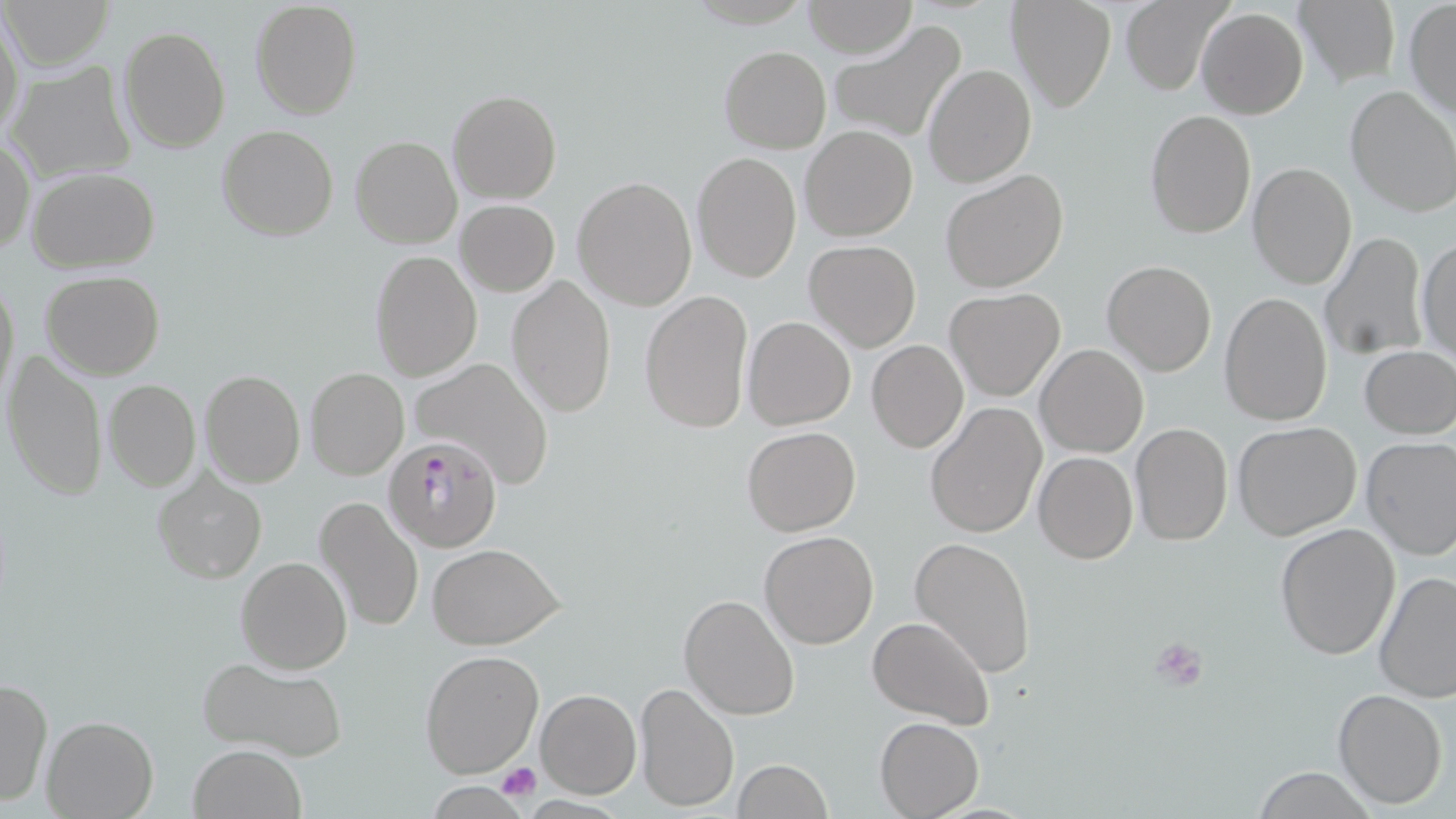 Approximate bounding boxes as (x1, y1, x2, y2) in pixels. Uninfected red blood cell locations: (3, 0, 115, 71), (1006, 0, 1117, 113), (1119, 0, 1229, 94), (1295, 0, 1399, 89), (250, 1, 362, 120), (802, 1, 917, 58), (1405, 2, 1455, 121), (1197, 7, 1308, 120), (0, 12, 24, 143), (826, 20, 968, 146), (118, 26, 231, 152), (718, 45, 831, 152), (5, 62, 137, 185), (923, 63, 1035, 187), (1344, 84, 1455, 218), (447, 89, 561, 204), (1143, 109, 1257, 239), (216, 125, 340, 241), (800, 126, 918, 242), (351, 136, 463, 250), (1, 139, 35, 256), (691, 151, 802, 284), (1247, 162, 1357, 289), (27, 167, 160, 273), (941, 170, 1069, 292), (573, 177, 697, 310), (456, 200, 559, 296), (1320, 232, 1428, 360), (1415, 237, 1455, 363), (804, 241, 921, 352), (370, 251, 483, 381), (1101, 260, 1217, 378), (40, 272, 164, 379), (506, 274, 616, 419), (1, 278, 19, 406), (944, 289, 1065, 401), (641, 290, 754, 437), (1219, 291, 1333, 427), (744, 317, 856, 430), (867, 340, 968, 452), (1035, 345, 1148, 459), (1360, 345, 1455, 440), (2, 348, 108, 502), (413, 358, 557, 483), (306, 367, 409, 479), (198, 369, 306, 488), (104, 380, 200, 491), (926, 403, 1046, 539), (1232, 421, 1362, 540), (1131, 423, 1233, 545), (742, 426, 861, 535), (1360, 436, 1456, 561), (1033, 451, 1138, 563), (151, 466, 266, 583), (315, 496, 424, 634), (1274, 521, 1402, 661), (758, 531, 879, 649), (909, 536, 1037, 676), (428, 543, 565, 648), (237, 554, 351, 674), (1373, 570, 1456, 706), (678, 593, 799, 720), (868, 617, 994, 729), (420, 649, 543, 777), (196, 653, 346, 759), (0, 677, 52, 807), (633, 681, 739, 813), (535, 688, 642, 799), (1331, 688, 1448, 810), (41, 715, 158, 819), (874, 717, 985, 818), (188, 744, 306, 819), (734, 759, 834, 819), (1250, 767, 1378, 818), (428, 783, 528, 817). Platelet locations: (1152, 638, 1207, 689), (496, 761, 541, 801). Plasmodium falciparum-infected red blood cell locations: (386, 437, 502, 553). Slide-level diagnosis: Plasmodium falciparum. 1000x magnification. Thin blood film. Image is 1456×819 pixels. One field of a larger specimen. May-Grünwald-Giemsa-stained preparation. Optical microscopy.